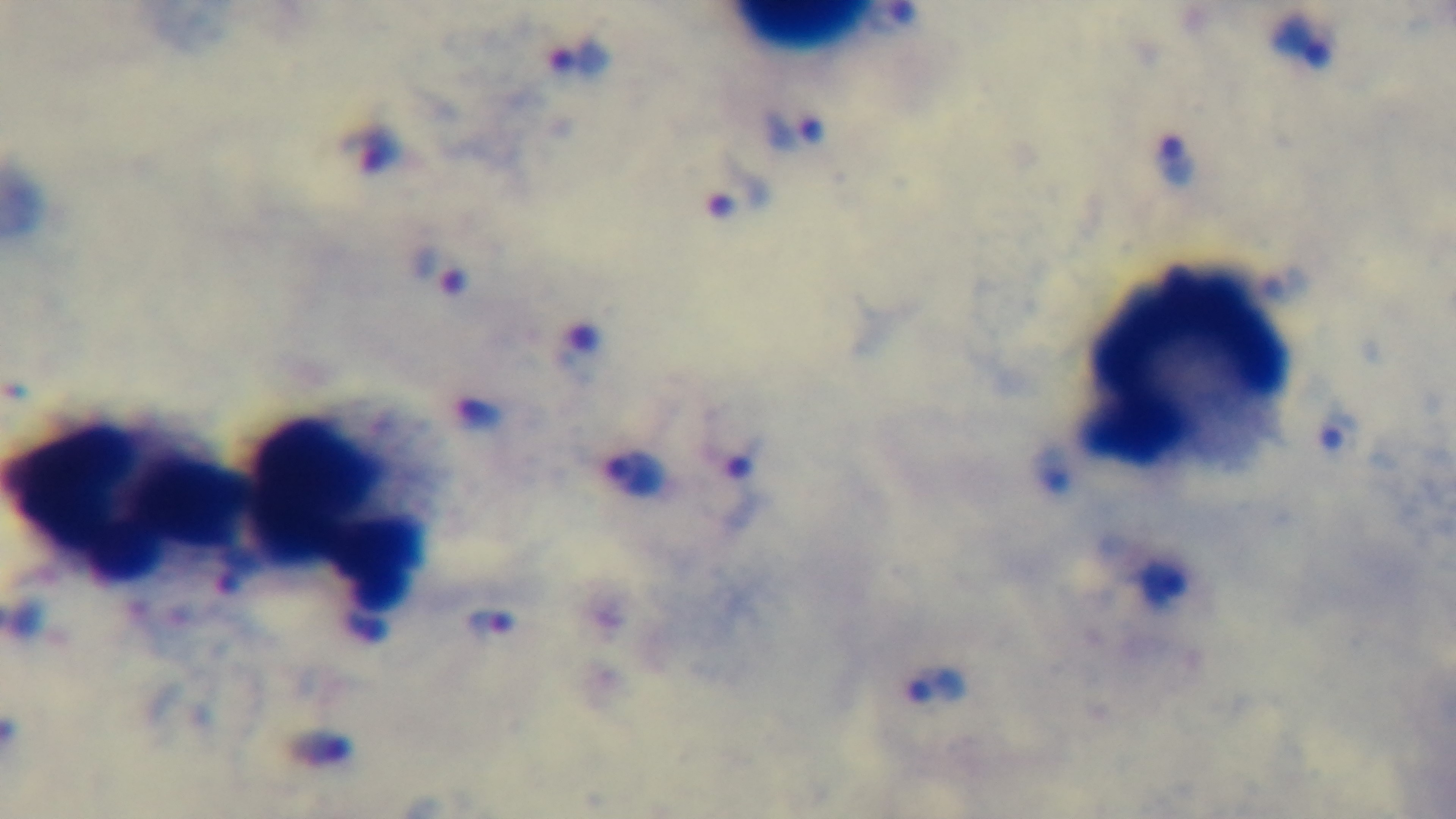

preparation = thick
modality = light microscopy
capture = mounted 4K digital camera
malaria status = positive
field of view = single
objective = 100x oil immersion
stain = Giemsa